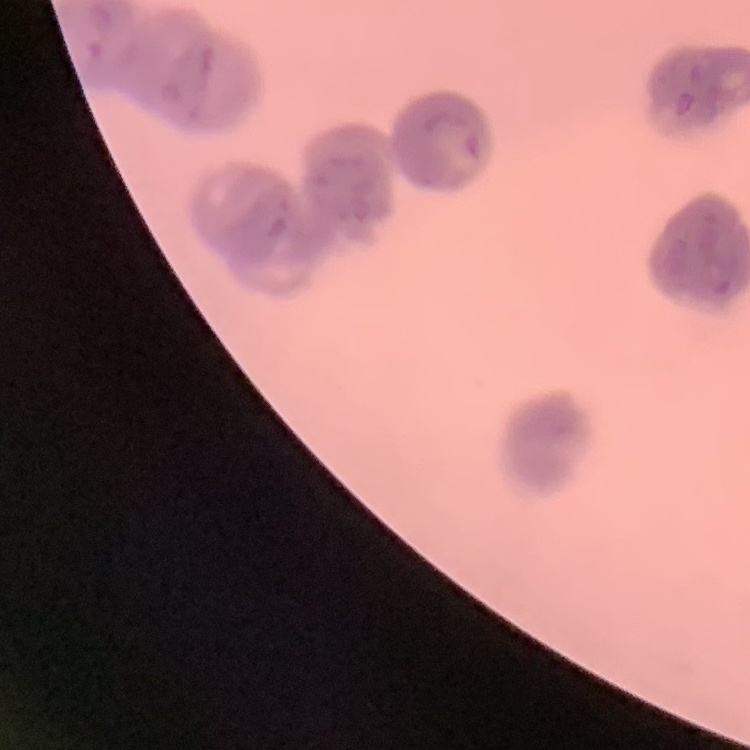
Summary:
  - Red blood cell morphology: rouleaux formation
  - Preparation: thin peripheral smear
  - Image type: one tile cut from a larger photomicrograph
  - Stain: Field's or Giemsa